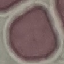 Malaria status: uninfected. Photographed with a smartphone camera at the microscope eyepiece. Cell patch, automatically extracted from a larger field of view and resized to 64 × 64 pixels. Giemsa-stained preparation. Thin blood film.